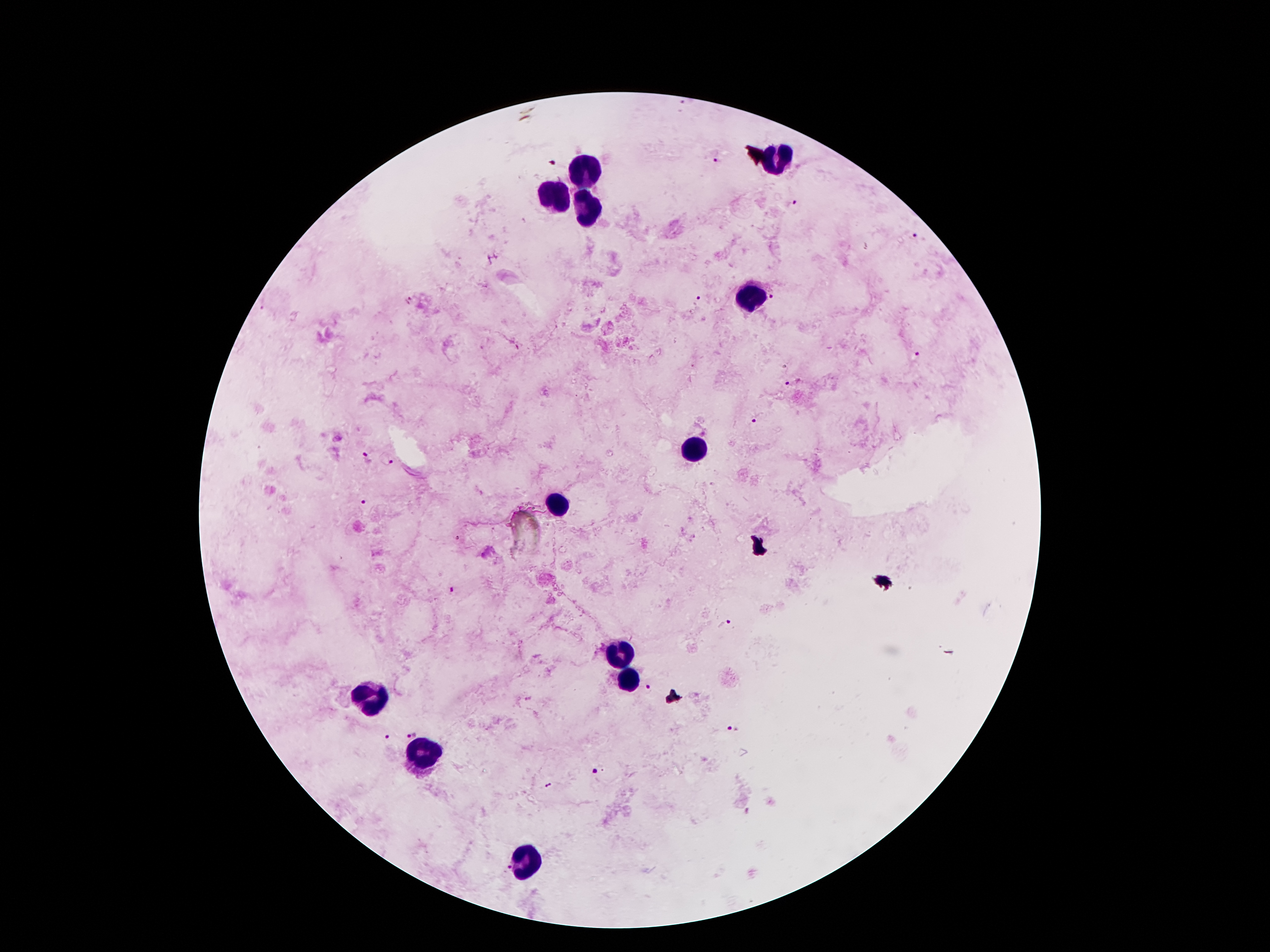

coordinate format = approximate centers as [x, y] in pixels
leukocyte locations = [781, 159], [586, 169], [561, 194], [588, 207], [756, 295], [692, 448], [559, 507], [617, 657], [627, 679], [373, 699], [420, 757], [527, 864]
malaria parasite locations = [717, 159], [552, 163], [797, 204], [919, 238], [699, 298], [776, 298], [407, 301], [917, 358], [793, 384], [757, 420], [368, 458], [389, 461], [362, 502], [454, 589], [725, 624], [650, 690], [733, 730], [411, 734], [387, 735], [597, 773], [505, 866]
image size = 1270×952 pixels
stain = Giemsa
patient malaria status = infected with Plasmodium falciparum
magnification = 100x
capture = smartphone camera through the microscope eyepiece
preparation = thick peripheral-blood smear
field of view = one from this slide